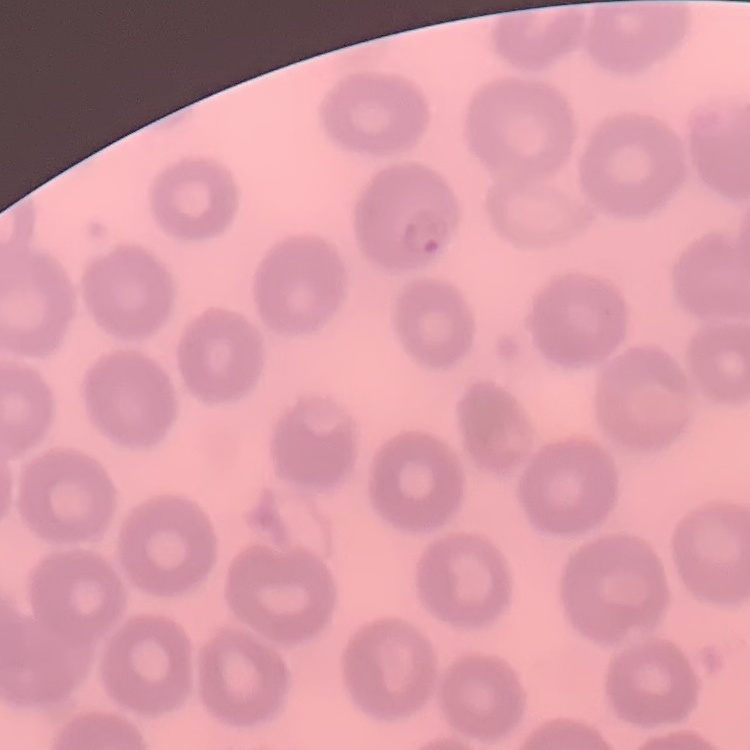
Summary:
  - Red blood cell morphology: no rouleaux formation
  - Stain: Field's or Giemsa
  - Image type: square crop of a larger photomicrograph
  - Preparation: thin blood film